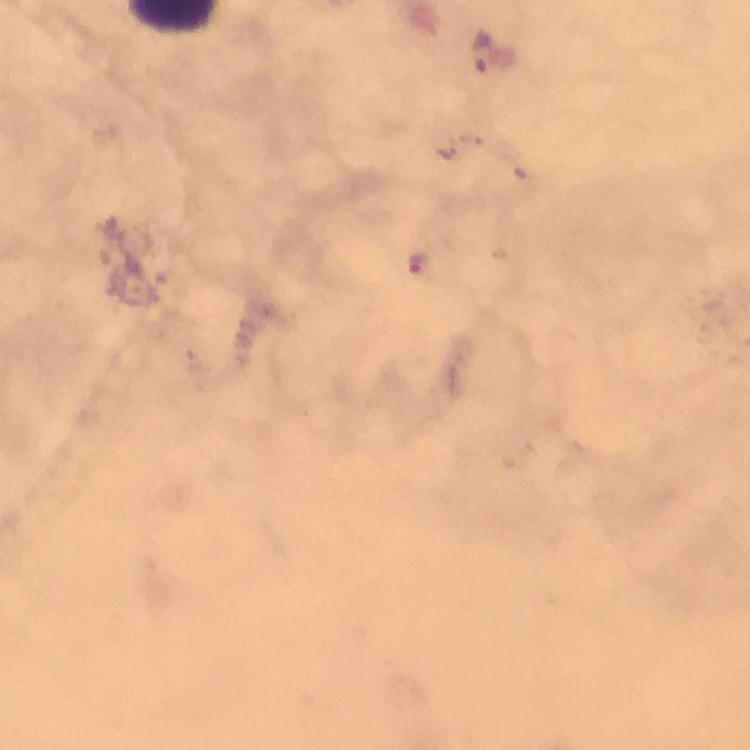

Approximate object centers, in pixels from the top-left corner.
Summary:
  - Plasmodium parasite locations: (x=482, y=49), (x=421, y=263)
  - Image size: 750×750 pixels
  - Stain: Giemsa
  - Magnification: 100x
  - Capture: smartphone mounted on the microscope
  - Context: from a diagnostic examination for malaria
  - Cropped from: one field of view
  - Immersion oil: used
  - Preparation: thick blood film